Give the extent of all Plasmodium falciparum-infected red blood cells.
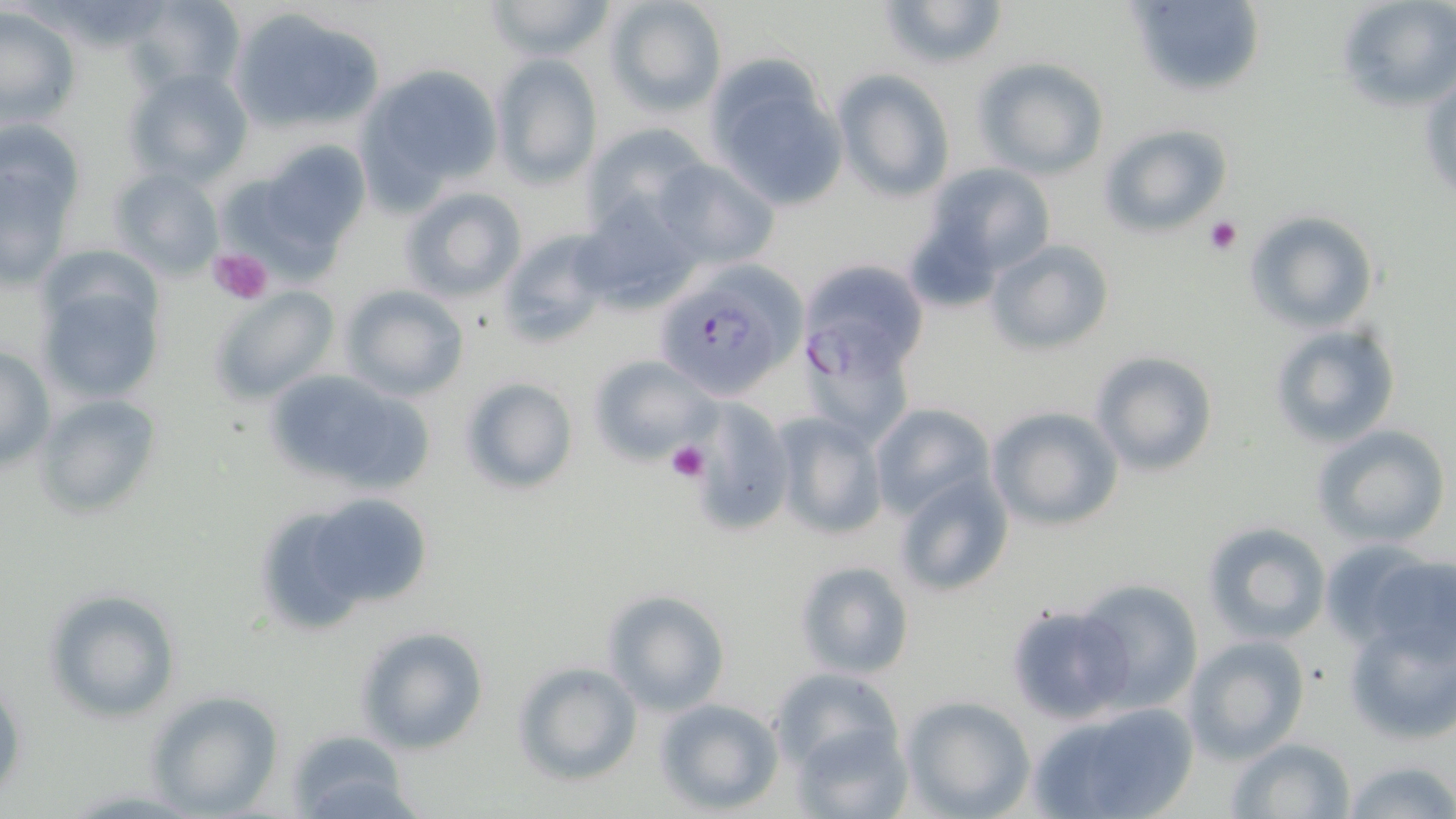

Approximate bounding boxes as (x1, y1, x2, y2) in pixels.
Plasmodium falciparum-infected red blood cells: (651, 261, 808, 402), (802, 264, 929, 391).

Summary:
  - Uninfected red blood cell locations: (126, 0, 246, 98), (481, 0, 617, 62), (603, 0, 725, 115), (876, 0, 1010, 71), (1334, 0, 1456, 116), (1123, 1, 1266, 96), (1, 6, 80, 129), (229, 8, 386, 135), (490, 51, 605, 187), (701, 54, 851, 211), (974, 57, 1110, 179), (360, 64, 502, 195), (124, 68, 252, 186), (835, 70, 954, 202), (1, 117, 85, 226), (1097, 122, 1233, 239), (579, 123, 709, 235), (262, 141, 370, 249), (1, 150, 77, 284), (653, 159, 778, 270), (924, 163, 1057, 279), (109, 167, 225, 279), (398, 185, 526, 303), (575, 194, 703, 312), (1245, 210, 1379, 332), (497, 229, 614, 347), (984, 239, 1115, 357), (36, 270, 167, 409), (339, 284, 469, 400), (213, 287, 339, 403), (1269, 322, 1404, 449), (804, 333, 913, 447), (0, 345, 54, 472), (1089, 350, 1220, 477), (588, 354, 718, 465), (268, 374, 434, 493), (459, 376, 578, 496), (36, 394, 163, 518), (689, 398, 793, 534), (869, 403, 996, 518), (987, 406, 1123, 532), (769, 412, 888, 542), (1312, 424, 1452, 549), (893, 471, 1013, 597), (307, 494, 432, 609), (1200, 522, 1329, 645), (1323, 541, 1456, 656), (793, 560, 917, 680), (1076, 578, 1203, 713), (44, 588, 181, 723), (602, 590, 730, 715), (1005, 602, 1132, 725), (1344, 615, 1455, 743), (356, 625, 488, 754), (1181, 635, 1310, 763), (511, 661, 642, 787), (767, 666, 907, 773), (1, 680, 27, 802), (143, 690, 282, 817), (901, 695, 1034, 818), (653, 698, 784, 816), (1027, 701, 1200, 819), (792, 721, 911, 819), (284, 731, 419, 818), (1230, 737, 1354, 818), (1340, 759, 1455, 819)
  - Platelet locations: (1204, 216, 1242, 254), (208, 246, 276, 307), (665, 441, 710, 484)
  - Slide-level diagnosis: Plasmodium falciparum
  - Magnification: 1000x
  - Preparation: thin blood smear
  - Stain: May-Grünwald-Giemsa
  - Modality: light microscopy
  - Image size: 1456×819 pixels
  - Field of view: single